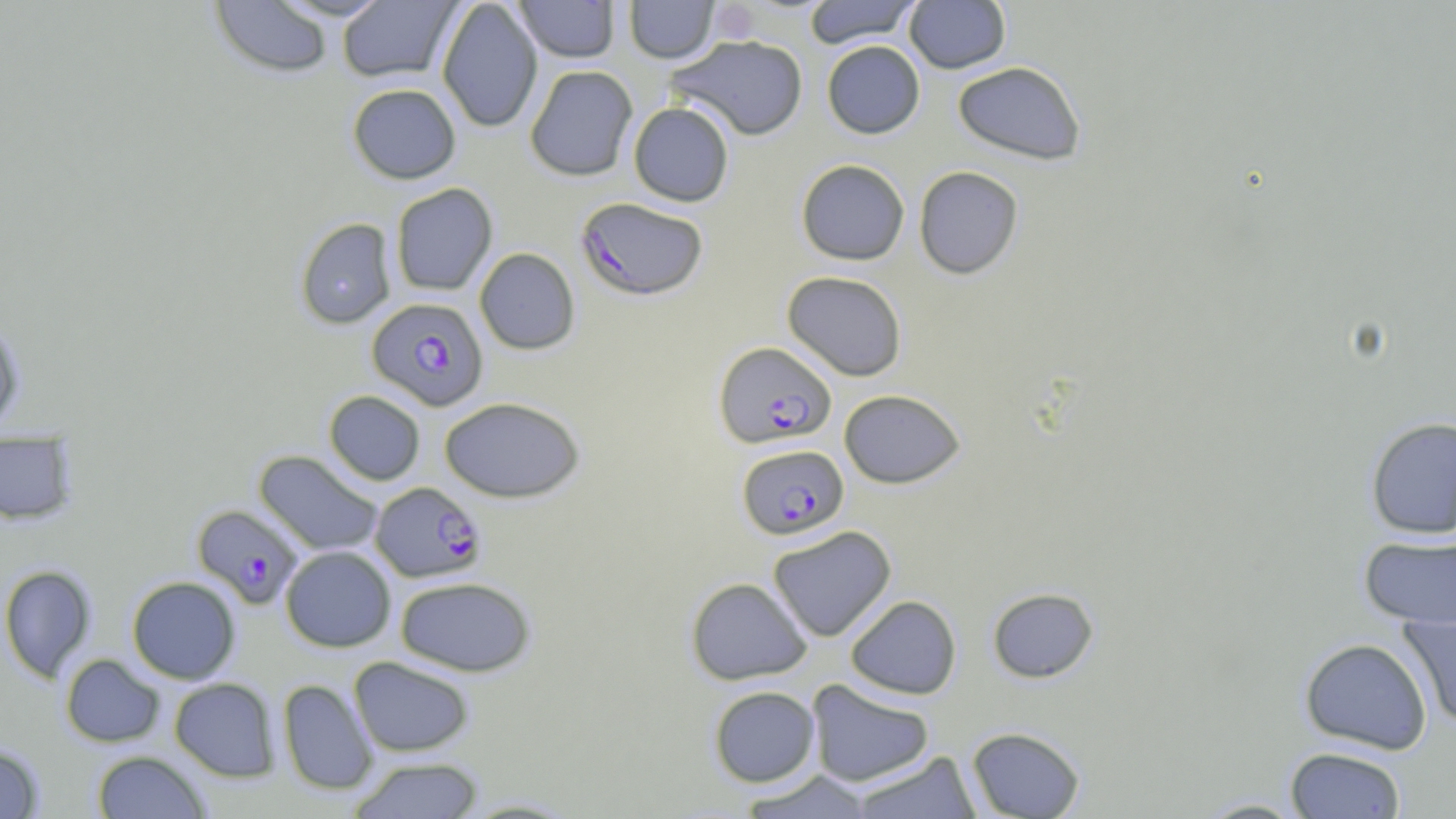
{
  "slide_level_diagnosis": "Plasmodium falciparum",
  "image_size": "1456×819 pixels",
  "field_of_view": "one of a larger specimen",
  "preparation": "thin blood smear",
  "stain": "May-Grünwald-Giemsa",
  "uninfected_red_blood_cell_locations": "approximate bounding boxes as [x1, y1, x2, y2] in pixels: [208, 0, 335, 79], [269, 0, 395, 21], [437, 0, 544, 134], [514, 0, 621, 63], [623, 0, 720, 63], [802, 0, 920, 49], [904, 0, 1011, 74], [337, 1, 462, 83], [667, 35, 809, 141], [821, 40, 925, 139], [953, 61, 1086, 165], [524, 65, 638, 182], [347, 83, 461, 184], [628, 102, 734, 207], [796, 159, 910, 265], [914, 165, 1024, 279], [390, 183, 498, 296], [294, 217, 397, 329], [474, 247, 580, 354], [783, 271, 908, 381], [0, 316, 26, 432], [839, 389, 965, 489], [324, 390, 425, 485], [439, 397, 586, 503], [1365, 416, 1456, 539], [0, 432, 78, 524], [253, 450, 385, 558], [768, 525, 897, 642], [1359, 533, 1456, 629], [280, 546, 396, 652], [0, 564, 97, 683], [127, 576, 241, 684], [395, 576, 537, 676], [685, 577, 813, 685], [986, 586, 1099, 683], [845, 595, 962, 699], [1399, 610, 1456, 729], [1299, 637, 1432, 755], [60, 654, 165, 747], [349, 656, 475, 757], [169, 678, 280, 781], [277, 678, 378, 796], [806, 679, 935, 787], [708, 685, 821, 787], [966, 726, 1085, 818], [0, 744, 46, 818], [1285, 746, 1406, 818], [92, 750, 210, 818], [849, 752, 982, 818], [350, 757, 484, 818], [737, 770, 877, 818], [455, 797, 586, 818], [1193, 798, 1311, 818]",
  "modality": "light microscopy",
  "plasmodium_falciparum_infected_red_blood_cell_locations": "approximate bounding boxes as [x1, y1, x2, y2] in pixels: [575, 197, 709, 301], [367, 297, 488, 411], [713, 341, 837, 449], [737, 444, 849, 540], [370, 482, 486, 582], [192, 503, 304, 609]",
  "magnification": "1000x"
}